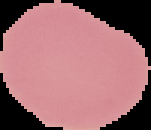 Malaria status: uninfected. Cell region segmented out of the field of view; the surrounding area is masked to black. From a thin blood smear. Image is 151×130 pixels.